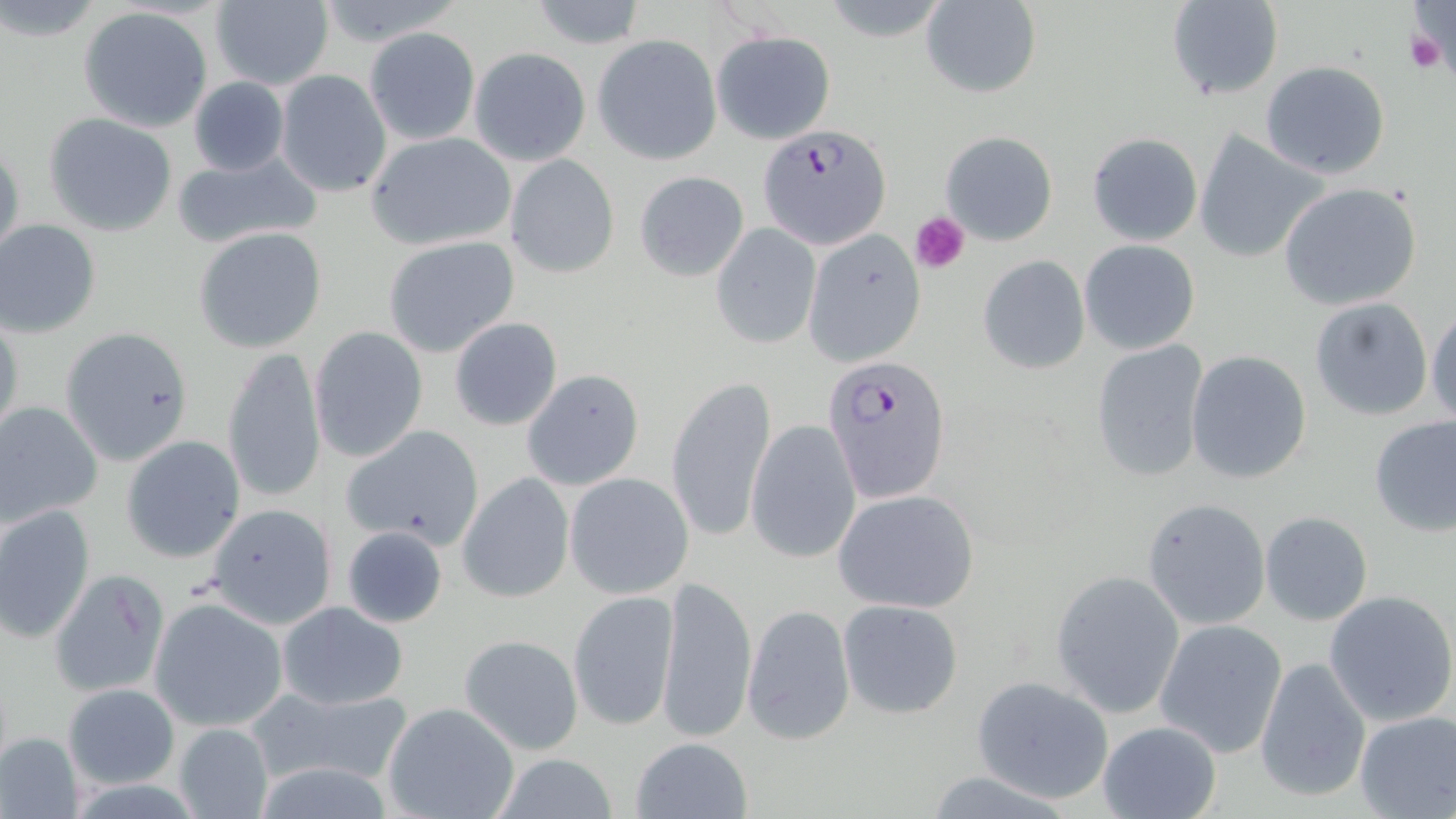
Summary:
  - Coordinate format: approximate bounding boxes as (x1,y1)-(x2,y2) corner pairs in pixels
  - Plasmodium falciparum-infected red blood cell locations: (757,123)-(892,251), (823,354)-(951,507)
  - Uninfected red blood cell locations: (312,0)-(467,49), (1166,0)-(1283,102), (1,1)-(102,43), (208,1)-(335,90), (528,1)-(647,49), (919,2)-(1042,99), (78,6)-(216,133), (364,27)-(481,144), (711,28)-(836,144), (594,35)-(722,164), (469,47)-(590,166), (1261,60)-(1390,179), (274,70)-(392,198), (188,77)-(289,177), (44,112)-(178,237), (1195,130)-(1327,265), (364,131)-(518,250), (940,131)-(1058,245), (1086,133)-(1203,246), (1,139)-(24,267), (171,150)-(325,250), (506,155)-(620,278), (634,170)-(749,282), (1279,182)-(1423,311), (0,220)-(101,338), (711,223)-(820,349), (193,226)-(329,353), (804,230)-(926,368), (382,237)-(520,358), (1079,240)-(1199,354), (978,255)-(1090,374), (1309,297)-(1433,420), (1427,302)-(1456,426), (0,311)-(24,446), (448,317)-(563,432), (309,326)-(430,465), (58,329)-(193,467), (1090,340)-(1209,483), (220,347)-(328,505), (1186,349)-(1312,484), (520,369)-(645,492), (665,375)-(777,543), (0,400)-(103,528), (1368,413)-(1456,536), (745,420)-(862,564), (339,423)-(486,551), (120,435)-(246,563), (457,472)-(576,604), (564,473)-(694,597), (833,489)-(979,612), (1141,498)-(1270,630), (205,502)-(337,628), (0,503)-(96,644), (1259,511)-(1372,626), (340,525)-(448,628), (49,568)-(170,699), (1051,570)-(1184,718), (655,572)-(755,745), (568,590)-(678,732), (1325,590)-(1456,726), (837,598)-(964,719), (151,600)-(288,731), (277,600)-(408,710), (741,603)-(856,745), (1155,619)-(1287,757), (458,633)-(584,754), (1256,654)-(1372,803), (972,675)-(1114,803), (64,683)-(179,788), (253,685)-(415,789), (382,700)-(521,819), (1353,709)-(1455,818), (1096,719)-(1221,819), (172,723)-(275,819), (0,731)-(84,819), (627,736)-(754,819), (486,754)-(625,818)
  - Platelet locations: (1407,29)-(1449,75), (912,211)-(971,272)
  - Slide-level diagnosis: Plasmodium falciparum
  - Magnification: 1000x
  - Field of view: single
  - Preparation: thin blood film
  - Modality: light microscopy
  - Stain: May-Grünwald-Giemsa
  - Image size: 1456×819 pixels